Classify this cell by malaria status.
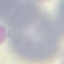
Uninfected.

preparation = thin smear
capture = smartphone camera at the microscope eyepiece
image type = automatically extracted cell patch, resized to 64 × 64 pixels
stain = Giemsa